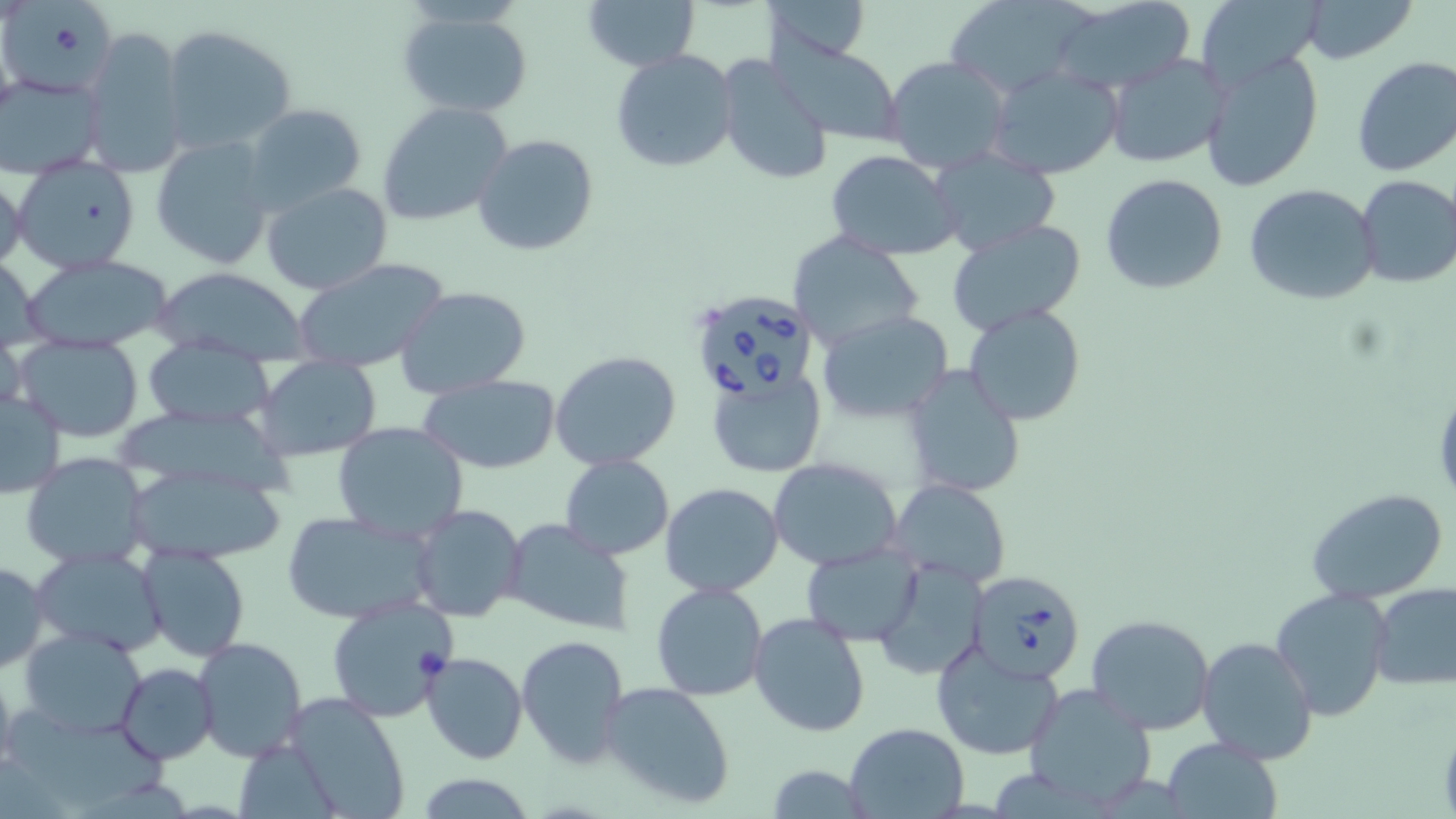

Approximate bounding boxes as (x1,y1)-(x2,y2) corner pairs in pixels. Uninfected red blood cell locations: (582,0)-(701,71), (763,0)-(870,63), (1046,0)-(1198,98), (1194,0)-(1327,93), (1300,0)-(1417,65), (944,1)-(1094,99), (6,5)-(119,97), (395,9)-(533,119), (161,24)-(297,155), (79,28)-(188,177), (767,37)-(905,145), (1200,48)-(1324,194), (612,49)-(739,174), (1105,52)-(1228,169), (883,56)-(1011,173), (1351,56)-(1456,177), (719,58)-(833,186), (982,66)-(1123,180), (0,73)-(104,180), (376,101)-(514,228), (242,103)-(368,212), (473,134)-(599,257), (150,136)-(274,270), (928,147)-(1062,257), (826,150)-(963,260), (12,159)-(143,273), (0,166)-(27,275), (1100,174)-(1229,295), (1355,175)-(1456,290), (260,182)-(394,296), (1243,183)-(1382,305), (946,219)-(1087,334), (789,232)-(925,350), (19,253)-(176,351), (0,254)-(46,351), (292,256)-(452,372), (151,267)-(311,360), (395,286)-(530,395), (964,305)-(1085,425), (819,310)-(952,423), (0,327)-(25,421), (15,336)-(146,440), (141,344)-(274,427), (550,350)-(681,471), (255,355)-(383,461), (902,365)-(1027,497), (706,370)-(825,481), (421,375)-(561,475), (1,389)-(67,498), (332,419)-(468,542), (21,453)-(151,568), (558,455)-(674,559), (768,457)-(905,571), (119,458)-(287,565), (889,479)-(1011,589), (660,483)-(785,599), (1305,489)-(1449,605), (409,504)-(525,622), (281,511)-(439,624), (500,517)-(634,636), (135,544)-(250,663), (799,544)-(924,646), (31,548)-(168,659), (875,557)-(989,679), (0,560)-(49,671), (650,582)-(770,702), (1371,582)-(1456,690), (1270,588)-(1396,720), (325,596)-(456,723), (748,613)-(870,736), (1086,613)-(1217,736), (18,626)-(149,737), (516,634)-(629,768), (190,635)-(308,763), (1195,636)-(1318,764), (931,639)-(1065,761), (421,651)-(528,764), (0,660)-(18,777), (118,663)-(218,764), (600,681)-(736,809), (1021,683)-(1157,810), (287,691)-(411,815), (843,721)-(968,818), (234,738)-(340,819), (1162,738)-(1284,818), (762,764)-(873,819), (412,774)-(539,817). Babesia divergens-infected red blood cell locations: (699,291)-(818,402), (972,568)-(1084,683). Slide-level diagnosis: Babesia divergens. Captured at 1000x magnification. Image is 1456×819 pixels. May-Grünwald-Giemsa stain. Single field of view. Optical microscopy. Thin blood film.